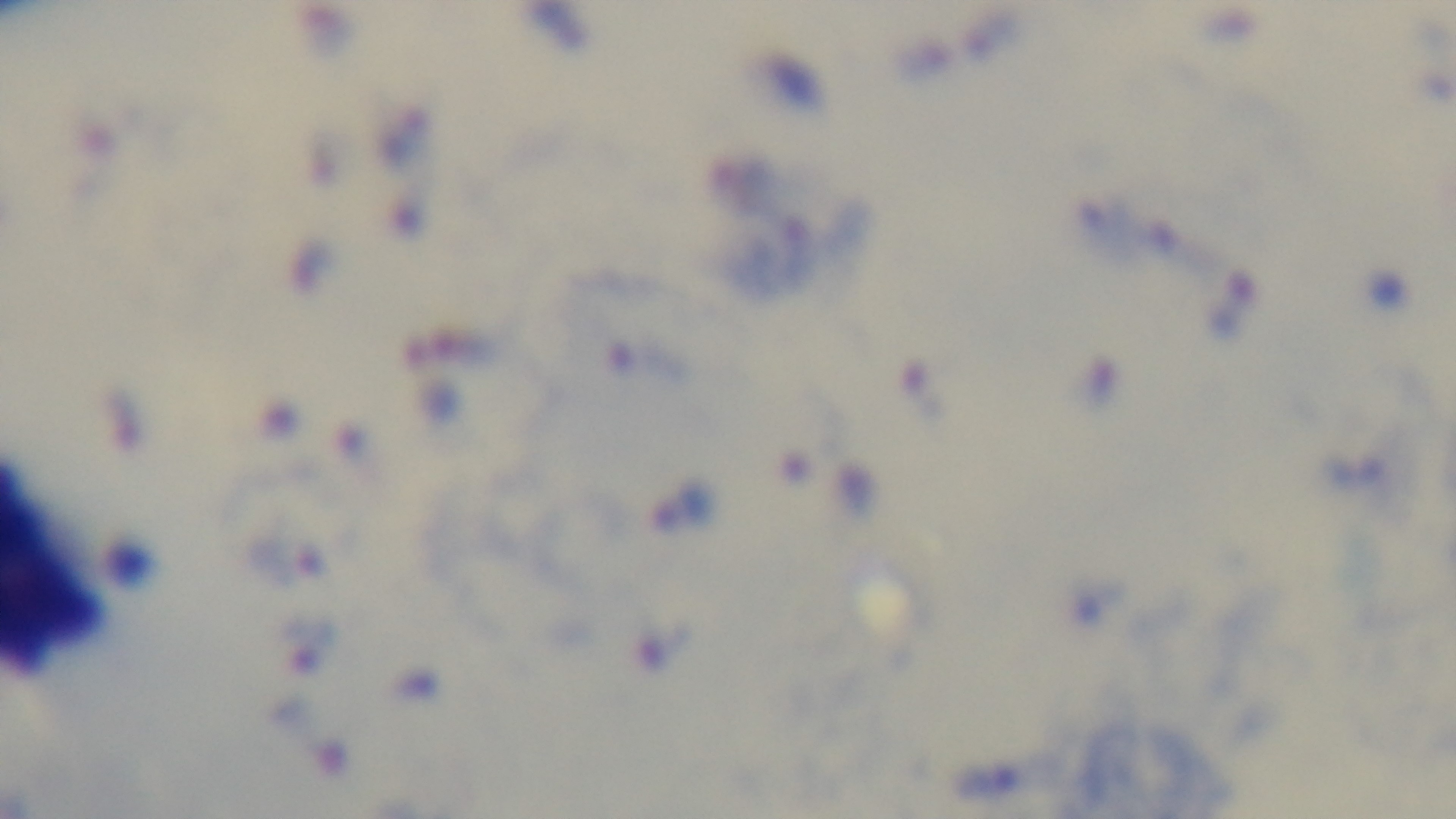
Summary:
  - Capture: mounted 4K digital camera
  - Objective: 100x oil immersion
  - Modality: light microscopy
  - Stain: Giemsa
  - Field of view: one from the slide
  - Malaria status: positive
  - Preparation: thick smear